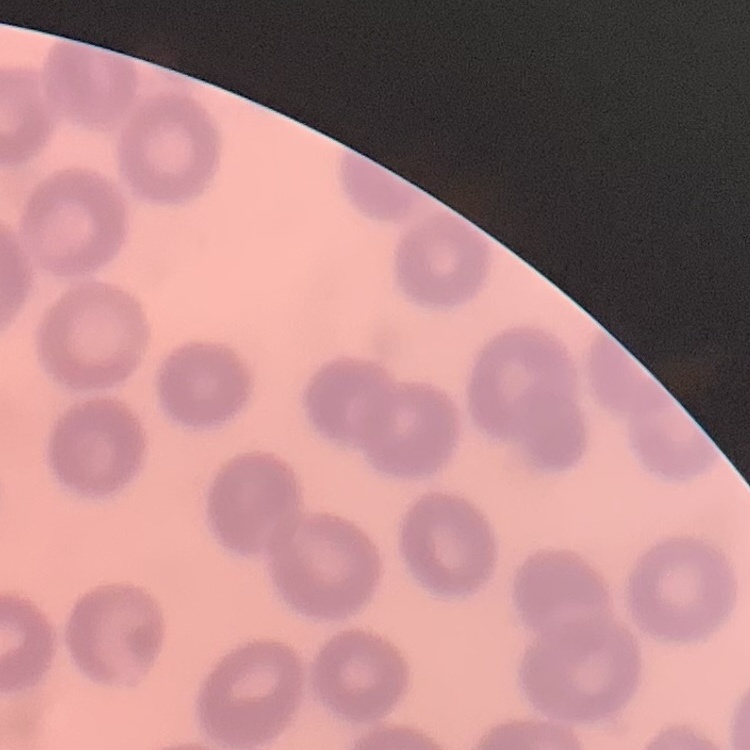 The erythrocytes exhibit no rouleaux formation. Square crop of a larger photomicrograph. Stained with either Field's or Giemsa. Thin peripheral smear.